Assess this cell for malaria.
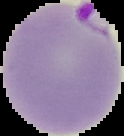

It is parasitized.

Image is 124×136 pixels. Segmented cell region on a black background. From a thin blood smear.